Classify this cell by malaria status.
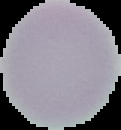

Uninfected.

From a thin blood film. The area outside the segmented cell region is set to black. Image is 121×130 pixels.